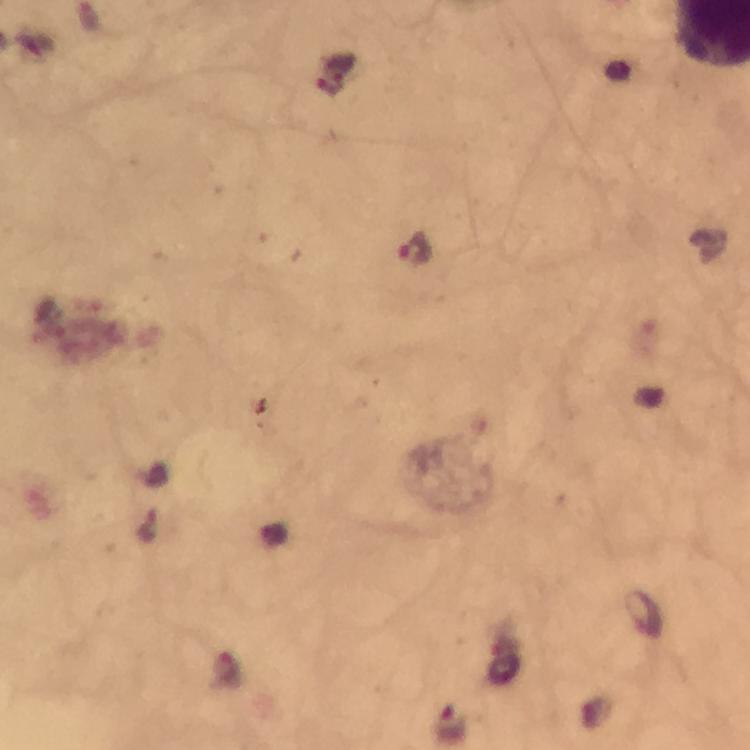
Approximate centers as (x, y) in pixels.
Summary:
  - Malaria parasite locations: (416, 247), (453, 726)
  - Context: from a malaria diagnostic workup
  - Image size: 750×750 pixels
  - Magnification: 100x
  - Stain: Giemsa
  - Cropped from: one field of view
  - Capture: smartphone camera through the microscope
  - Immersion oil: used
  - Preparation: thick blood film